Report the malaria status of this cell.
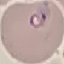
It is parasitized.

capture = smartphone through the microscope eyepiece
image type = cell patch, automatically extracted from a larger field of view and resized to 64 × 64 pixels
stain = Giemsa
preparation = thin smear